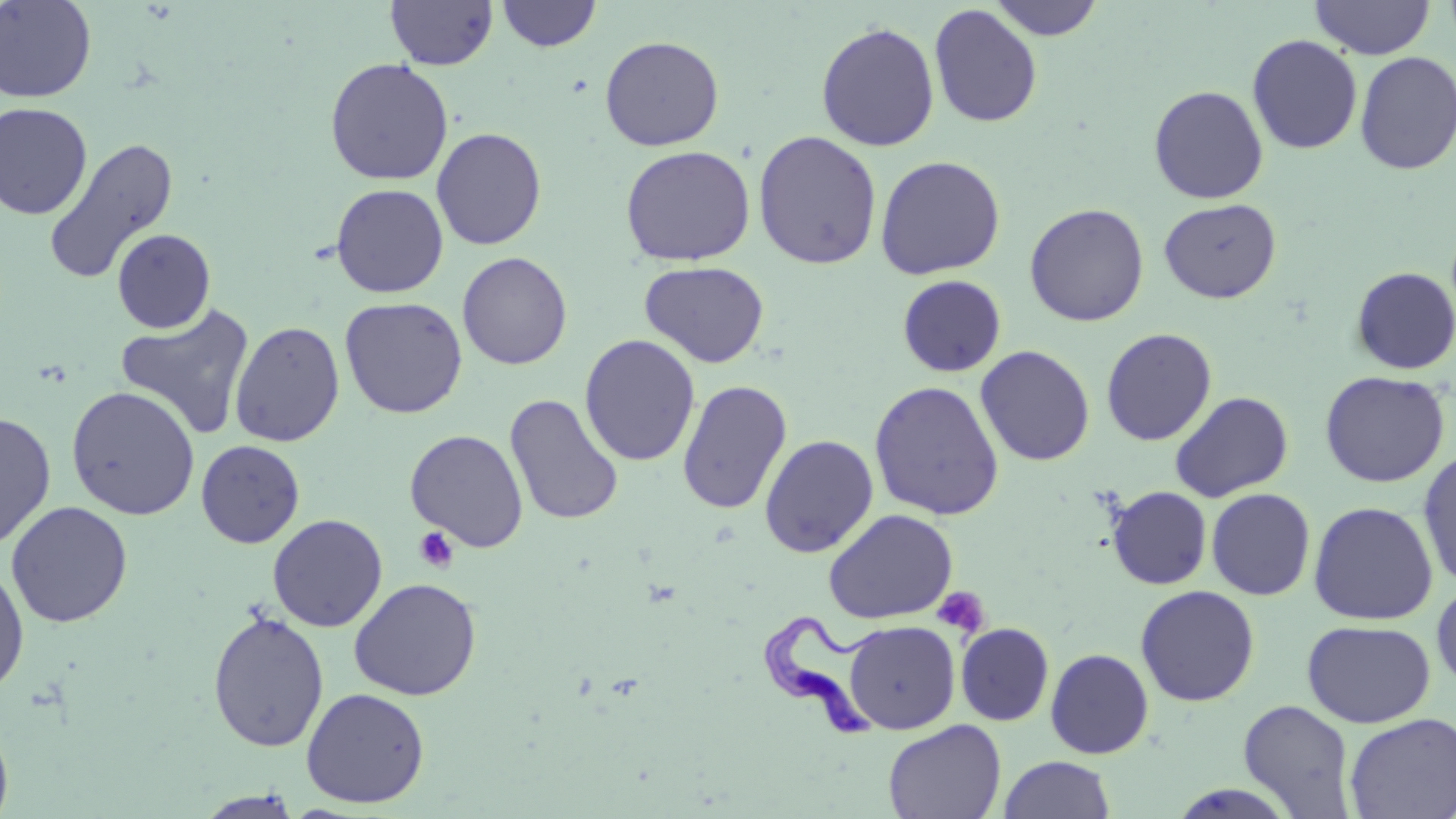 Approximate bounding boxes as [x1, y1, x2, y2] in pixels. Trypanosoma brucei locations: [759, 609, 886, 740]. Uninfected red blood cell locations: [0, 0, 97, 103], [385, 0, 498, 70], [497, 0, 602, 52], [990, 0, 1104, 41], [1310, 1, 1435, 59], [929, 4, 1043, 129], [816, 22, 940, 152], [1247, 34, 1363, 154], [599, 36, 725, 151], [1354, 51, 1456, 175], [325, 57, 454, 185], [1148, 85, 1269, 204], [0, 102, 93, 220], [430, 127, 547, 251], [752, 130, 883, 270], [43, 137, 179, 285], [619, 145, 756, 266], [875, 155, 1006, 280], [330, 183, 449, 298], [1159, 198, 1281, 303], [1024, 202, 1149, 327], [112, 228, 215, 333], [457, 252, 572, 370], [639, 261, 770, 368], [1351, 266, 1456, 375], [896, 275, 1007, 377], [340, 297, 468, 419], [115, 302, 256, 441], [229, 321, 345, 447], [1100, 328, 1217, 446], [579, 334, 701, 467], [975, 345, 1095, 467], [1319, 370, 1451, 487], [677, 379, 792, 514], [869, 380, 1005, 521], [65, 386, 200, 520], [1169, 391, 1293, 502], [504, 394, 624, 526], [0, 412, 56, 551], [405, 429, 528, 552], [759, 434, 878, 558], [196, 440, 305, 548], [1417, 448, 1456, 590], [1106, 486, 1212, 590], [1205, 488, 1316, 600], [6, 500, 132, 628], [1308, 501, 1438, 625], [823, 508, 958, 624], [267, 513, 388, 632], [0, 562, 30, 696], [348, 577, 482, 701], [1431, 579, 1456, 694], [1135, 585, 1260, 706], [207, 610, 329, 752], [1301, 619, 1435, 728], [844, 620, 960, 734], [956, 623, 1054, 725], [1045, 649, 1154, 759], [301, 687, 430, 808], [1238, 699, 1356, 817], [1343, 712, 1456, 819], [0, 713, 14, 819], [883, 718, 1006, 819], [999, 755, 1115, 818], [195, 790, 306, 818]. Platelet locations: [413, 527, 460, 573], [932, 586, 990, 639]. Slide-level diagnosis: Trypanosoma brucei. Single field of view. Image is 1456×819 pixels. Light microscopy. May-Grünwald-Giemsa stain. Thin blood film. 1000x magnification.